Report the malaria status of this cell.
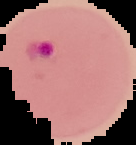

Parasitized.

image type = cell region segmented out of the field of view; surrounding area masked to black
image size = 136×145 pixels
preparation = thin blood smear